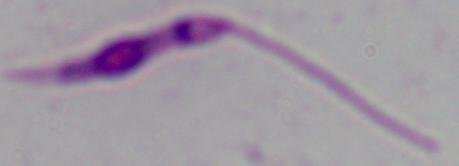 1000x magnification. Micrograph. A Leishmania parasite is seen.